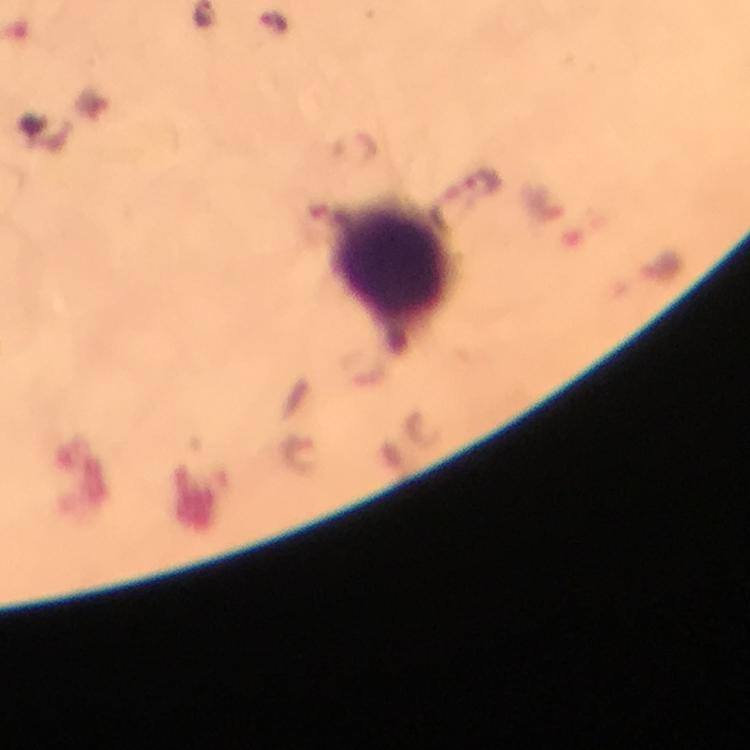

Approximate centers as (x, y) in pixels.
Summary:
  - Leukocyte locations: (390, 267)
  - Plasmodium parasite locations: (485, 181)
  - Preparation: thick blood film
  - Immersion oil: used
  - Image size: 750×750 pixels
  - Cropped from: a single field of view
  - Capture: smartphone photograph through a microscope
  - Context: from a malaria diagnostic workup
  - Stain: Giemsa
  - Magnification: 100x